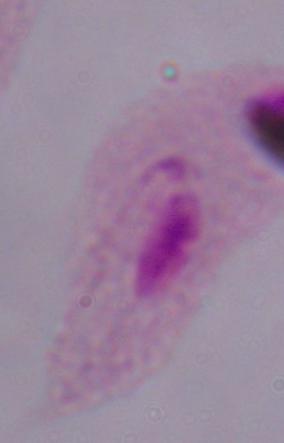

Photomicrograph. 1000x magnification. A trichomonad is shown.